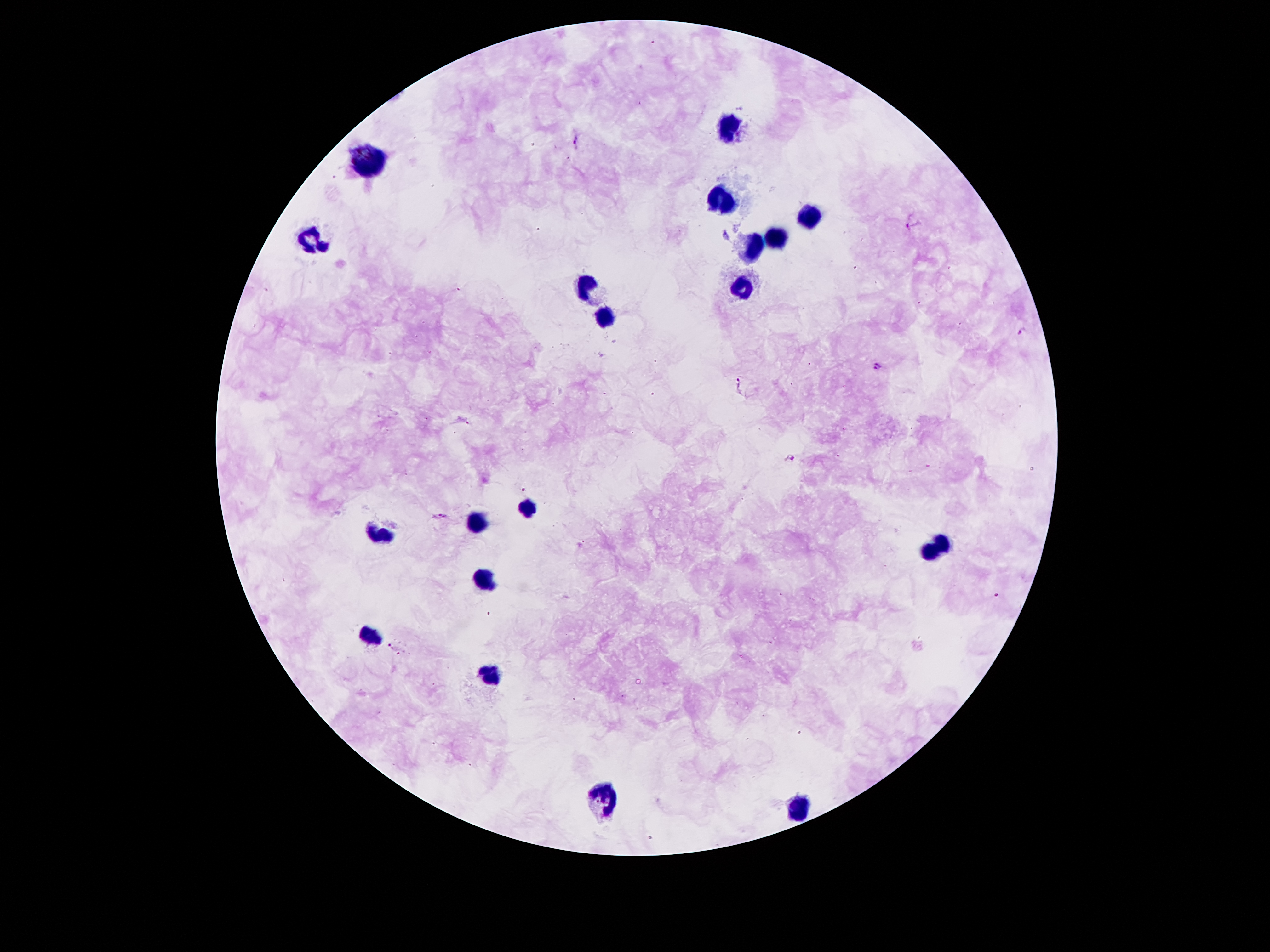

Approximate object centers, in pixels from the top-left corner.
Summary:
  - Leukocyte locations: (x=731, y=131), (x=374, y=158), (x=720, y=200), (x=808, y=216), (x=771, y=237), (x=314, y=240), (x=750, y=241), (x=584, y=285), (x=741, y=286), (x=610, y=316), (x=521, y=506), (x=477, y=523), (x=374, y=535), (x=949, y=541), (x=932, y=550), (x=482, y=580), (x=370, y=634), (x=486, y=673), (x=605, y=799), (x=799, y=806)
  - Malaria parasite locations: (x=576, y=139), (x=912, y=225), (x=1022, y=331), (x=876, y=366), (x=737, y=383), (x=791, y=457), (x=440, y=517), (x=395, y=650)
  - Magnification: 100x
  - Stain: Giemsa
  - Preparation: thick blood smear
  - Patient malaria status: positive for Plasmodium falciparum
  - Field of view: single
  - Capture: smartphone through the microscope eyepiece
  - Image size: 1270×952 pixels